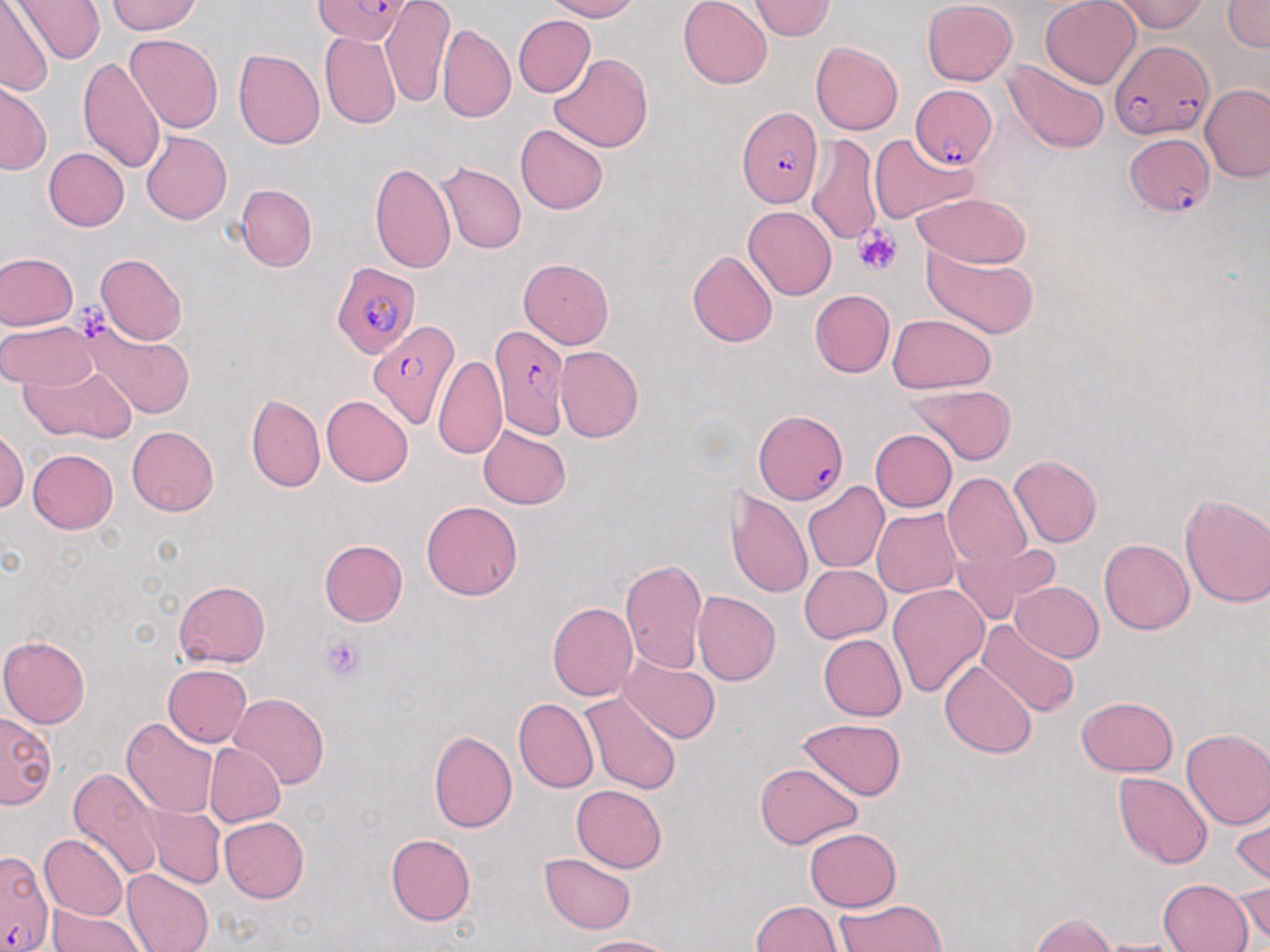 Approximate bounding boxes as named x1/y1/x2/y2 corners in pixels. Uninfected red blood cell locations: (x1=13, y1=0, x2=106, y2=68), (x1=545, y1=0, x2=641, y2=21), (x1=678, y1=0, x2=772, y2=89), (x1=1040, y1=0, x2=1141, y2=88), (x1=1111, y1=0, x2=1209, y2=33), (x1=1222, y1=0, x2=1270, y2=52), (x1=106, y1=1, x2=203, y2=35), (x1=380, y1=1, x2=453, y2=108), (x1=747, y1=1, x2=835, y2=40), (x1=922, y1=1, x2=1019, y2=86), (x1=0, y1=3, x2=54, y2=95), (x1=513, y1=15, x2=595, y2=98), (x1=437, y1=23, x2=515, y2=122), (x1=320, y1=31, x2=401, y2=130), (x1=124, y1=33, x2=223, y2=134), (x1=811, y1=42, x2=903, y2=136), (x1=233, y1=49, x2=325, y2=150), (x1=549, y1=53, x2=652, y2=152), (x1=78, y1=56, x2=166, y2=175), (x1=1003, y1=59, x2=1110, y2=154), (x1=0, y1=78, x2=50, y2=175), (x1=1199, y1=83, x2=1270, y2=181), (x1=515, y1=124, x2=608, y2=214), (x1=141, y1=132, x2=232, y2=225), (x1=869, y1=133, x2=976, y2=225), (x1=805, y1=134, x2=881, y2=247), (x1=43, y1=147, x2=129, y2=232), (x1=368, y1=161, x2=457, y2=274), (x1=437, y1=162, x2=526, y2=254), (x1=235, y1=183, x2=316, y2=272), (x1=910, y1=192, x2=1032, y2=268), (x1=743, y1=205, x2=837, y2=300), (x1=923, y1=248, x2=1039, y2=339), (x1=687, y1=250, x2=778, y2=346), (x1=1, y1=252, x2=78, y2=330), (x1=96, y1=253, x2=187, y2=345), (x1=518, y1=258, x2=614, y2=348), (x1=810, y1=289, x2=894, y2=377), (x1=886, y1=313, x2=997, y2=393), (x1=79, y1=320, x2=196, y2=421), (x1=1, y1=321, x2=98, y2=390), (x1=556, y1=346, x2=644, y2=442), (x1=433, y1=355, x2=507, y2=460), (x1=23, y1=364, x2=136, y2=443), (x1=908, y1=384, x2=1018, y2=464), (x1=247, y1=395, x2=325, y2=493), (x1=321, y1=395, x2=415, y2=486), (x1=477, y1=425, x2=572, y2=509), (x1=126, y1=426, x2=220, y2=516), (x1=0, y1=427, x2=28, y2=513), (x1=869, y1=429, x2=957, y2=512), (x1=27, y1=449, x2=118, y2=534), (x1=1010, y1=455, x2=1102, y2=547), (x1=942, y1=473, x2=1031, y2=569), (x1=802, y1=482, x2=889, y2=574), (x1=725, y1=487, x2=813, y2=598), (x1=1178, y1=491, x2=1270, y2=609), (x1=421, y1=500, x2=523, y2=601), (x1=872, y1=508, x2=962, y2=598), (x1=1099, y1=538, x2=1193, y2=634), (x1=318, y1=540, x2=407, y2=627), (x1=953, y1=543, x2=1059, y2=619), (x1=619, y1=557, x2=708, y2=673), (x1=799, y1=564, x2=890, y2=642), (x1=173, y1=580, x2=270, y2=666), (x1=1010, y1=582, x2=1104, y2=662), (x1=888, y1=583, x2=990, y2=697), (x1=692, y1=591, x2=781, y2=687), (x1=547, y1=601, x2=638, y2=702), (x1=976, y1=621, x2=1081, y2=720), (x1=818, y1=634, x2=906, y2=721), (x1=0, y1=635, x2=91, y2=727), (x1=619, y1=654, x2=720, y2=743), (x1=941, y1=661, x2=1036, y2=758), (x1=162, y1=664, x2=252, y2=747), (x1=229, y1=692, x2=329, y2=788), (x1=576, y1=693, x2=683, y2=795), (x1=1076, y1=696, x2=1179, y2=775), (x1=513, y1=697, x2=599, y2=793), (x1=0, y1=710, x2=56, y2=809), (x1=121, y1=717, x2=220, y2=818), (x1=796, y1=718, x2=907, y2=801), (x1=1181, y1=728, x2=1270, y2=829), (x1=429, y1=729, x2=517, y2=833), (x1=203, y1=742, x2=285, y2=828), (x1=755, y1=762, x2=862, y2=849), (x1=68, y1=768, x2=164, y2=880), (x1=1112, y1=772, x2=1215, y2=869), (x1=571, y1=784, x2=667, y2=872), (x1=1232, y1=799, x2=1270, y2=889), (x1=141, y1=803, x2=225, y2=889), (x1=219, y1=816, x2=309, y2=903), (x1=804, y1=827, x2=902, y2=911), (x1=40, y1=834, x2=128, y2=920), (x1=385, y1=834, x2=477, y2=926), (x1=539, y1=853, x2=637, y2=934), (x1=121, y1=868, x2=215, y2=951), (x1=1235, y1=876, x2=1270, y2=945), (x1=1157, y1=878, x2=1253, y2=951), (x1=835, y1=899, x2=947, y2=951), (x1=750, y1=900, x2=844, y2=951), (x1=46, y1=904, x2=145, y2=952), (x1=1031, y1=912, x2=1118, y2=951), (x1=574, y1=936, x2=679, y2=952), (x1=1091, y1=937, x2=1192, y2=951). Platelet locations: (x1=855, y1=225, x2=903, y2=275), (x1=69, y1=297, x2=114, y2=342), (x1=321, y1=635, x2=365, y2=681). Plasmodium falciparum-infected red blood cell locations: (x1=312, y1=0, x2=414, y2=46), (x1=1112, y1=42, x2=1213, y2=145), (x1=910, y1=86, x2=998, y2=169), (x1=735, y1=105, x2=823, y2=208), (x1=1124, y1=132, x2=1213, y2=218), (x1=332, y1=264, x2=419, y2=359), (x1=367, y1=318, x2=461, y2=430), (x1=491, y1=324, x2=570, y2=441), (x1=754, y1=408, x2=848, y2=506), (x1=0, y1=850, x2=55, y2=951). Slide-level diagnosis: Plasmodium falciparum. Thin blood film. May-Grünwald-Giemsa stain. Captured at 1000x magnification. Image is 1270×952 pixels. Single field of view. Optical microscopy.